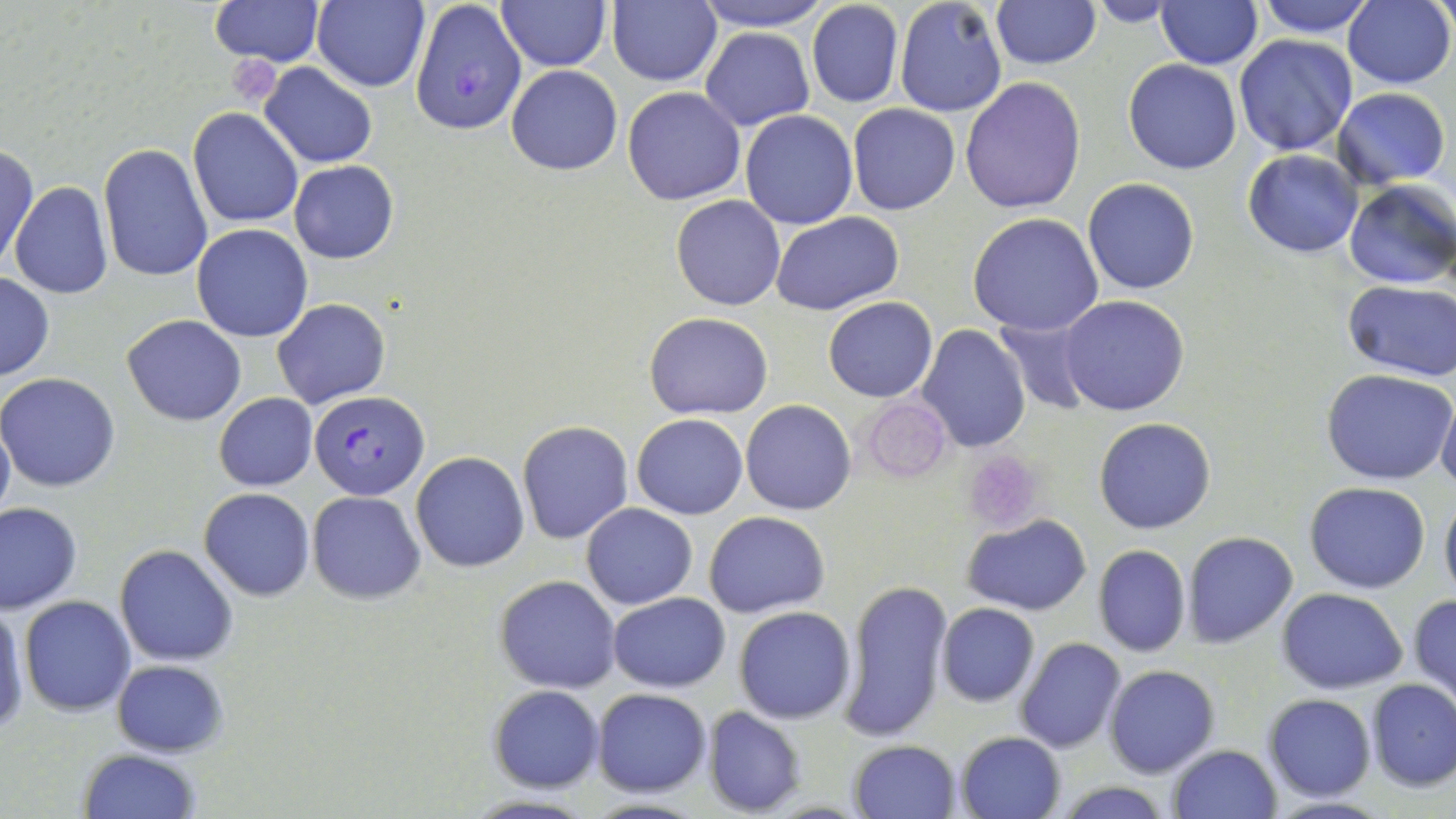

Approximate bounding boxes as named x1/y1/x2/y2 corners in pixels. Plasmodium falciparum-infected red blood cell locations: (x1=410, y1=1, x2=527, y2=136), (x1=312, y1=389, x2=428, y2=501). Platelet locations: (x1=223, y1=59, x2=283, y2=102), (x1=861, y1=395, x2=950, y2=483), (x1=962, y1=451, x2=1044, y2=533). Uninfected red blood cell locations: (x1=210, y1=0, x2=323, y2=67), (x1=313, y1=0, x2=431, y2=93), (x1=608, y1=0, x2=723, y2=87), (x1=690, y1=0, x2=832, y2=30), (x1=893, y1=0, x2=1008, y2=119), (x1=1254, y1=0, x2=1378, y2=38), (x1=499, y1=1, x2=609, y2=72), (x1=805, y1=1, x2=905, y2=109), (x1=991, y1=1, x2=1101, y2=71), (x1=1083, y1=1, x2=1185, y2=27), (x1=1343, y1=1, x2=1455, y2=89), (x1=1156, y1=2, x2=1262, y2=70), (x1=699, y1=27, x2=815, y2=130), (x1=1234, y1=35, x2=1360, y2=157), (x1=1122, y1=59, x2=1242, y2=175), (x1=260, y1=63, x2=378, y2=166), (x1=507, y1=64, x2=622, y2=175), (x1=960, y1=77, x2=1088, y2=214), (x1=623, y1=86, x2=745, y2=205), (x1=1333, y1=87, x2=1451, y2=186), (x1=847, y1=104, x2=960, y2=215), (x1=188, y1=109, x2=305, y2=227), (x1=738, y1=109, x2=859, y2=230), (x1=1, y1=142, x2=38, y2=272), (x1=98, y1=143, x2=212, y2=283), (x1=1242, y1=149, x2=1365, y2=258), (x1=289, y1=160, x2=399, y2=264), (x1=1083, y1=178, x2=1200, y2=294), (x1=1342, y1=179, x2=1456, y2=290), (x1=10, y1=182, x2=113, y2=301), (x1=672, y1=194, x2=786, y2=311), (x1=772, y1=212, x2=900, y2=314), (x1=968, y1=213, x2=1104, y2=336), (x1=192, y1=224, x2=313, y2=343), (x1=0, y1=273, x2=54, y2=381), (x1=1341, y1=282, x2=1456, y2=380), (x1=1058, y1=294, x2=1190, y2=416), (x1=823, y1=297, x2=938, y2=402), (x1=272, y1=298, x2=391, y2=409), (x1=645, y1=313, x2=773, y2=420), (x1=122, y1=314, x2=246, y2=425), (x1=990, y1=314, x2=1096, y2=414), (x1=916, y1=325, x2=1031, y2=451), (x1=1319, y1=366, x2=1455, y2=485), (x1=0, y1=372, x2=121, y2=492), (x1=1437, y1=389, x2=1456, y2=495), (x1=213, y1=393, x2=317, y2=491), (x1=740, y1=400, x2=856, y2=516), (x1=0, y1=411, x2=15, y2=528), (x1=632, y1=413, x2=747, y2=520), (x1=1093, y1=417, x2=1216, y2=533), (x1=516, y1=420, x2=634, y2=544), (x1=410, y1=452, x2=528, y2=572), (x1=1304, y1=480, x2=1431, y2=595), (x1=200, y1=488, x2=315, y2=601), (x1=1439, y1=490, x2=1456, y2=603), (x1=308, y1=492, x2=425, y2=605), (x1=1, y1=502, x2=83, y2=612), (x1=581, y1=502, x2=697, y2=609), (x1=704, y1=510, x2=831, y2=619), (x1=964, y1=512, x2=1090, y2=615), (x1=1182, y1=531, x2=1298, y2=648), (x1=1093, y1=544, x2=1191, y2=656), (x1=115, y1=545, x2=239, y2=665), (x1=495, y1=574, x2=622, y2=694), (x1=840, y1=577, x2=952, y2=742), (x1=1277, y1=588, x2=1408, y2=694), (x1=1409, y1=592, x2=1456, y2=709), (x1=608, y1=593, x2=731, y2=690), (x1=20, y1=595, x2=134, y2=715), (x1=937, y1=603, x2=1038, y2=707), (x1=0, y1=605, x2=27, y2=736), (x1=733, y1=606, x2=857, y2=724), (x1=1015, y1=638, x2=1126, y2=753), (x1=111, y1=659, x2=228, y2=756), (x1=1104, y1=664, x2=1218, y2=778), (x1=1365, y1=678, x2=1456, y2=793), (x1=489, y1=685, x2=604, y2=792), (x1=592, y1=687, x2=712, y2=797), (x1=1263, y1=693, x2=1376, y2=802), (x1=701, y1=705, x2=807, y2=817), (x1=955, y1=732, x2=1066, y2=819), (x1=849, y1=738, x2=961, y2=818), (x1=1167, y1=744, x2=1281, y2=819), (x1=78, y1=749, x2=201, y2=819), (x1=1049, y1=781, x2=1179, y2=817), (x1=462, y1=794, x2=599, y2=818). Slide-level diagnosis: Plasmodium falciparum. Image is 1456×819 pixels. Optical microscopy. Captured at 1000x magnification. One field of a larger specimen. May-Grünwald-Giemsa stain. Thin blood smear.